State the preparation type.
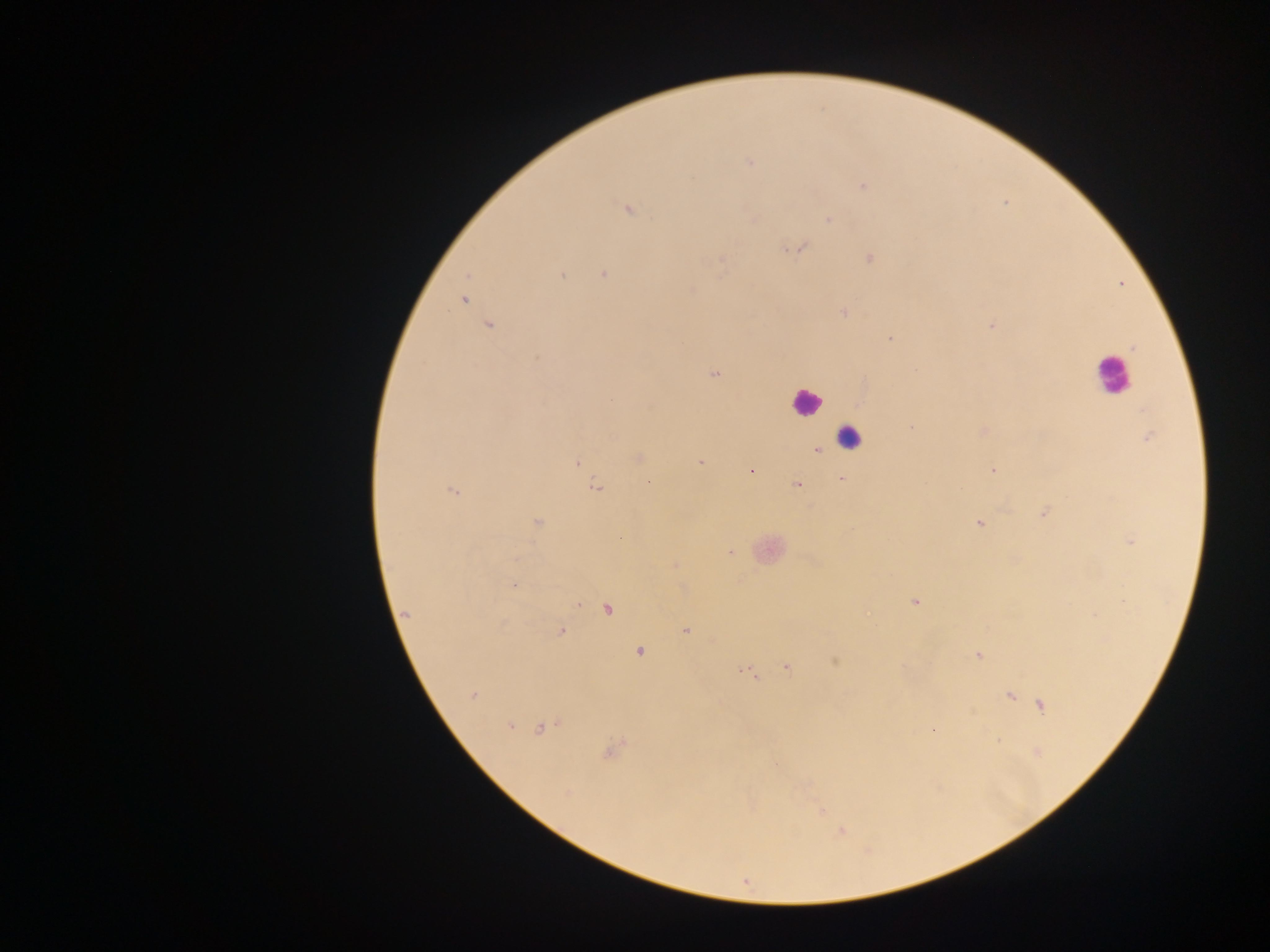

This is a thick smear.

Approximate centers as [x, y] in pixels.
Summary:
  - Leukocyte locations: [1110, 374], [806, 402], [849, 438], [772, 549]
  - Malaria parasite locations: [749, 162], [863, 186], [629, 209], [828, 220], [799, 248], [870, 258], [721, 260], [603, 274], [562, 276], [692, 291], [463, 300], [845, 312], [490, 326], [992, 326], [890, 339], [1134, 348], [714, 374], [911, 427], [1147, 437], [817, 451], [639, 459], [699, 461], [576, 463], [993, 469], [751, 470], [841, 478], [797, 485], [597, 487], [454, 491], [1044, 513], [537, 523], [980, 524], [1131, 542], [730, 553], [676, 564], [513, 586], [915, 602], [579, 604], [607, 610], [407, 614], [686, 631], [560, 632], [639, 652], [979, 655], [835, 662], [787, 668], [747, 672], [472, 696], [1011, 696], [1041, 705], [510, 727], [543, 728], [933, 731], [998, 740], [612, 752], [1036, 752], [776, 766], [567, 793], [821, 811], [842, 832]
  - Capture: mobile-phone photograph through a microscope
  - Field of view: single
  - Country: Ghana
  - Image size: 1270×952 pixels